Classify this cell by malaria status.
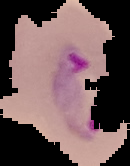
It is parasitized.

preparation = thin blood film
image type = cell region segmented out of the field of view; surrounding area masked to black
image size = 130×166 pixels